Describe the morphology of the red blood cells.
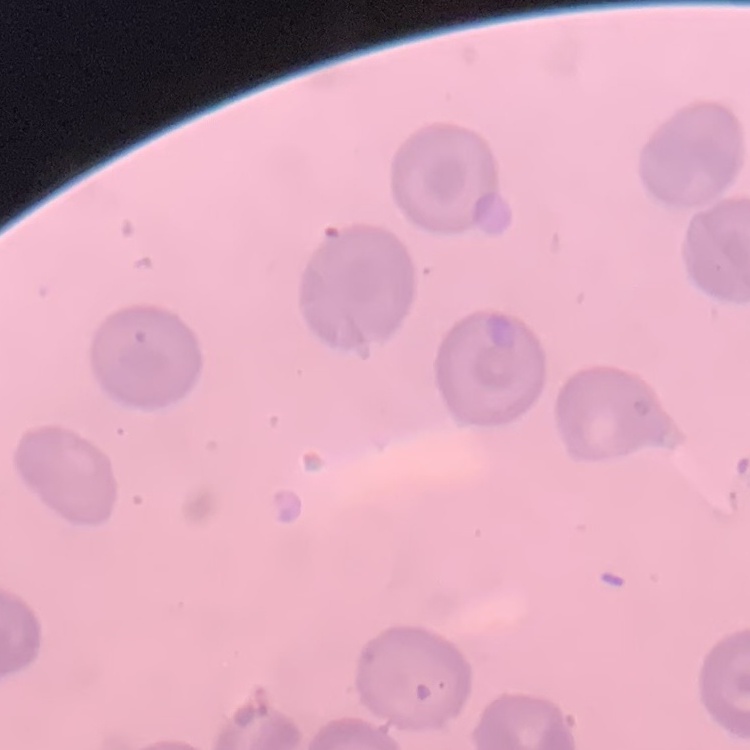
No rouleaux formation.

image type = square crop of a larger photomicrograph
preparation = thin peripheral smear
stain = Field's or Giemsa